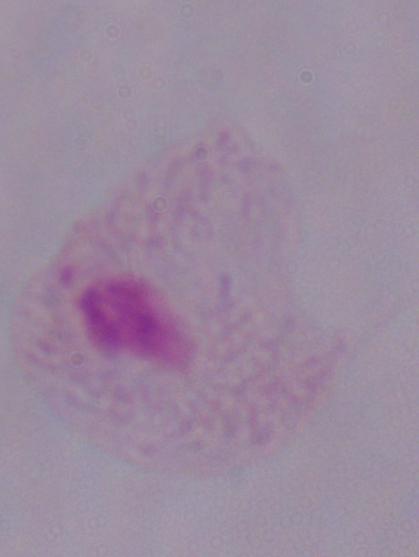

A trichomonad is seen. Micrograph. Captured at 1000x magnification.